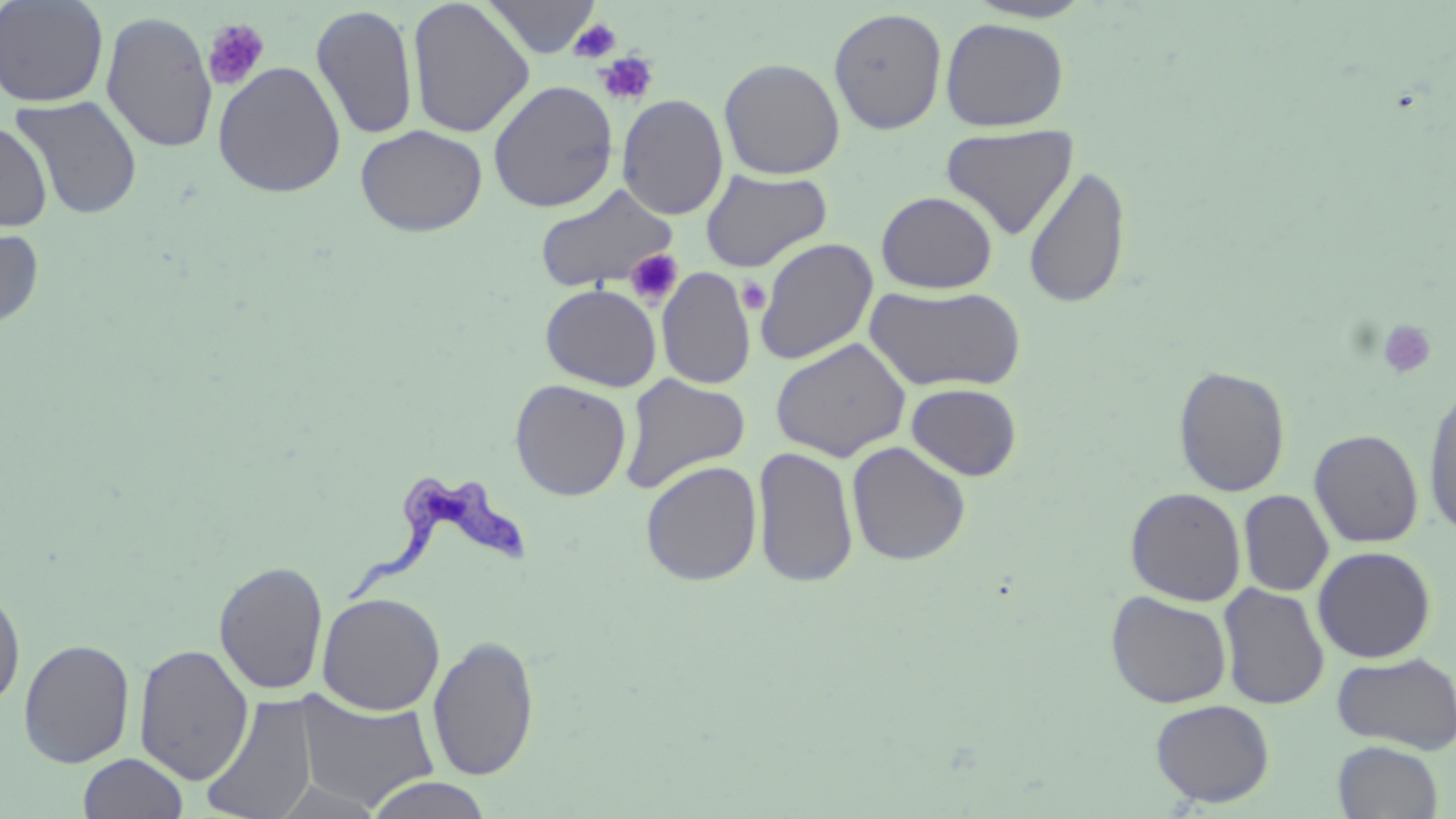

Trypanosoma brucei locations = approximate bounding boxes as named x1/y1/x2/y2 corners in pixels: (x1=339, y1=474, x2=536, y2=602)
slide-level diagnosis = Trypanosoma brucei
platelet locations = approximate bounding boxes as named x1/y1/x2/y2 corners in pixels: (x1=569, y1=17, x2=622, y2=63), (x1=202, y1=18, x2=271, y2=92), (x1=594, y1=51, x2=659, y2=106), (x1=626, y1=248, x2=684, y2=307), (x1=737, y1=277, x2=772, y2=315), (x1=1378, y1=319, x2=1437, y2=379)
modality = optical microscopy
stain = May-Grünwald-Giemsa
preparation = thin blood film
image size = 1456×819 pixels
magnification = 1000x
uninfected red blood cell locations = approximate bounding boxes as named x1/y1/x2/y2 corners in pixels: (x1=0, y1=0, x2=109, y2=107), (x1=483, y1=0, x2=602, y2=58), (x1=407, y1=1, x2=534, y2=138), (x1=963, y1=1, x2=1097, y2=23), (x1=311, y1=4, x2=419, y2=141), (x1=828, y1=7, x2=947, y2=135), (x1=101, y1=11, x2=218, y2=154), (x1=940, y1=17, x2=1069, y2=132), (x1=719, y1=58, x2=845, y2=179), (x1=212, y1=61, x2=346, y2=198), (x1=488, y1=80, x2=618, y2=213), (x1=10, y1=93, x2=144, y2=219), (x1=617, y1=94, x2=729, y2=220), (x1=0, y1=120, x2=53, y2=232), (x1=941, y1=123, x2=1079, y2=240), (x1=355, y1=124, x2=487, y2=236), (x1=1022, y1=165, x2=1130, y2=309), (x1=701, y1=168, x2=832, y2=272), (x1=534, y1=183, x2=679, y2=294), (x1=876, y1=190, x2=998, y2=294), (x1=0, y1=225, x2=44, y2=328), (x1=754, y1=237, x2=879, y2=365), (x1=657, y1=267, x2=756, y2=390), (x1=540, y1=283, x2=662, y2=391), (x1=864, y1=284, x2=1026, y2=393), (x1=769, y1=337, x2=911, y2=461), (x1=1173, y1=366, x2=1291, y2=497), (x1=619, y1=373, x2=751, y2=494), (x1=509, y1=379, x2=632, y2=501), (x1=1423, y1=382, x2=1456, y2=542), (x1=906, y1=383, x2=1022, y2=481), (x1=1309, y1=429, x2=1424, y2=548), (x1=846, y1=441, x2=971, y2=566), (x1=751, y1=445, x2=860, y2=589), (x1=641, y1=460, x2=763, y2=586), (x1=1125, y1=486, x2=1247, y2=606), (x1=1238, y1=490, x2=1333, y2=597), (x1=1312, y1=546, x2=1436, y2=663), (x1=213, y1=559, x2=329, y2=696), (x1=1218, y1=583, x2=1329, y2=710), (x1=0, y1=584, x2=26, y2=712), (x1=1106, y1=590, x2=1233, y2=708), (x1=317, y1=592, x2=445, y2=716), (x1=428, y1=634, x2=540, y2=781), (x1=18, y1=638, x2=135, y2=768), (x1=134, y1=643, x2=254, y2=784), (x1=1332, y1=652, x2=1456, y2=754), (x1=293, y1=691, x2=439, y2=811), (x1=201, y1=695, x2=319, y2=819), (x1=1150, y1=699, x2=1275, y2=807), (x1=1332, y1=740, x2=1444, y2=818), (x1=78, y1=752, x2=188, y2=818), (x1=365, y1=776, x2=494, y2=818), (x1=272, y1=780, x2=386, y2=818)
field of view = single